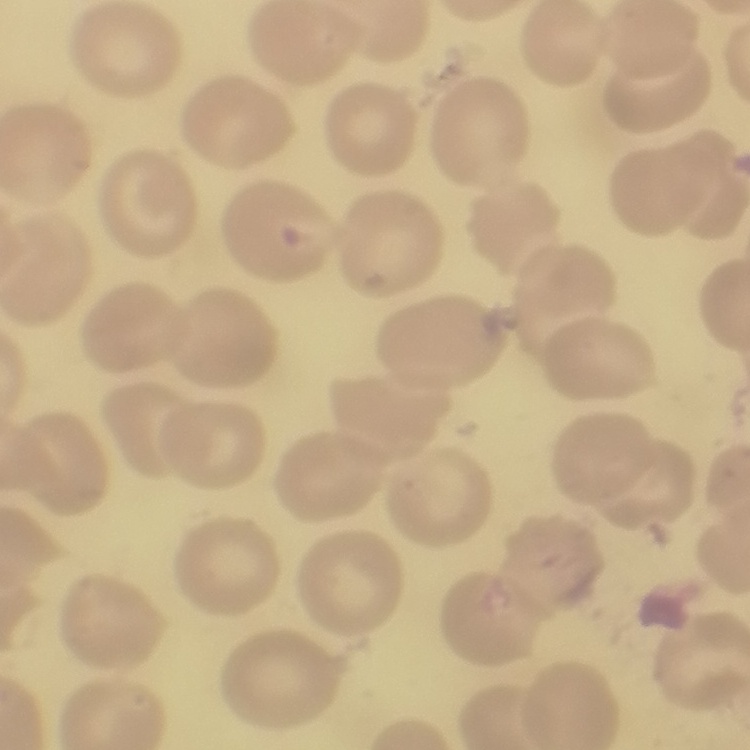
red blood cell morphology = no rouleaux formation
stain = Field's or Giemsa
image type = one tile cut from a larger photomicrograph
preparation = thin blood film